Give the position of every Plasmodium parasite visible.
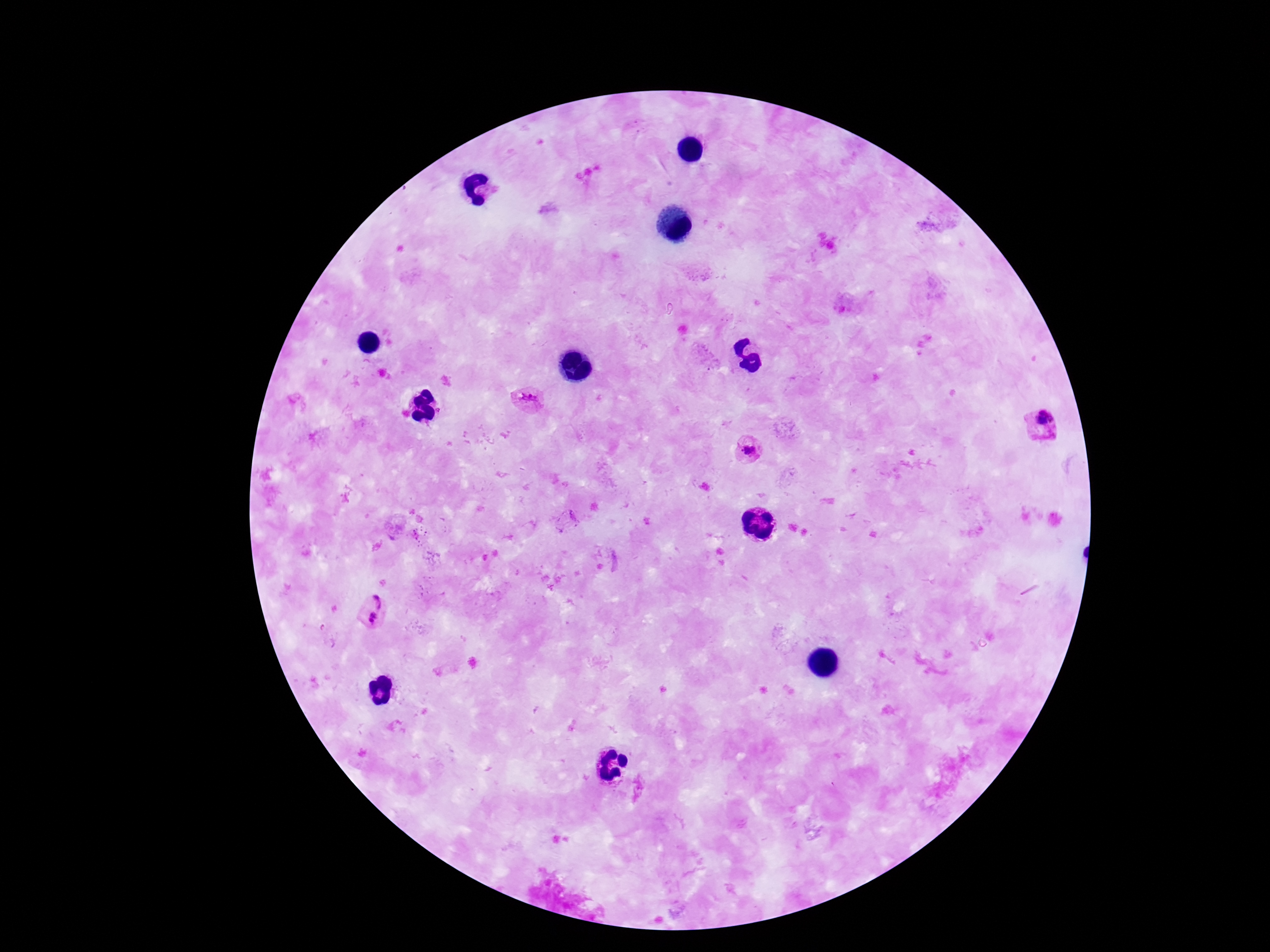

Approximate centers as [x, y] in pixels.
Plasmodium parasites: [531, 400], [1045, 422], [749, 451], [379, 598], [372, 621], [639, 789].

Summary:
  - Image size: 1270×952 pixels
  - Stain: Giemsa
  - Capture: smartphone camera through the microscope eyepiece
  - Preparation: thick blood smear
  - Patient malaria status: infected
  - Field of view: single
  - Magnification: 100x